Give the position of every malaria parasite.
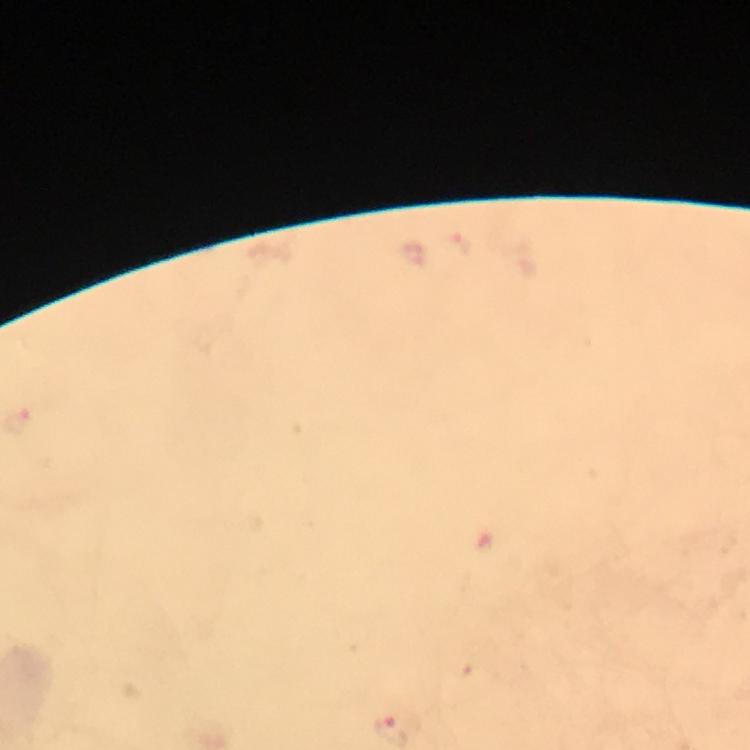
Approximate centers as (x, y) in pixels.
Malaria parasites: (462, 241).

From a diagnostic examination for malaria. 100x magnification. Cropped region of a single field of view. Immersion oil was used. Image is 750×750 pixels. Thick smear. Giemsa stain. Smartphone photograph taken through a microscope.